Report the malaria status of this cell.
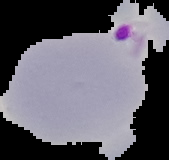

It is parasitized.

Summary:
  - Preparation: thin blood film
  - Image size: 169×160 pixels
  - Image type: segmented cell region with the area outside set to black